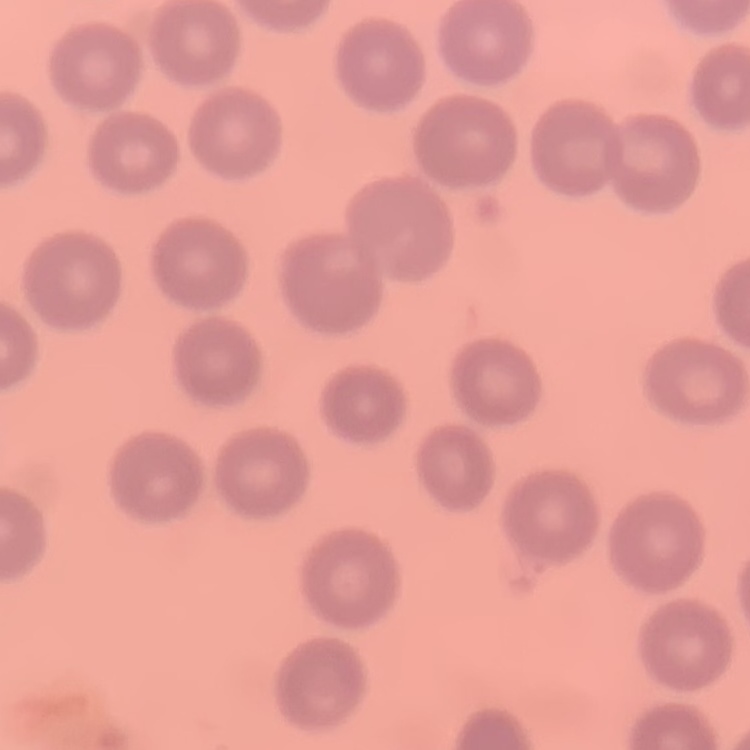
Summary:
  - Red blood cell morphology: no rouleaux formation
  - Preparation: thin blood smear
  - Stain: Field's or Giemsa
  - Image type: one tile cut from a larger photomicrograph